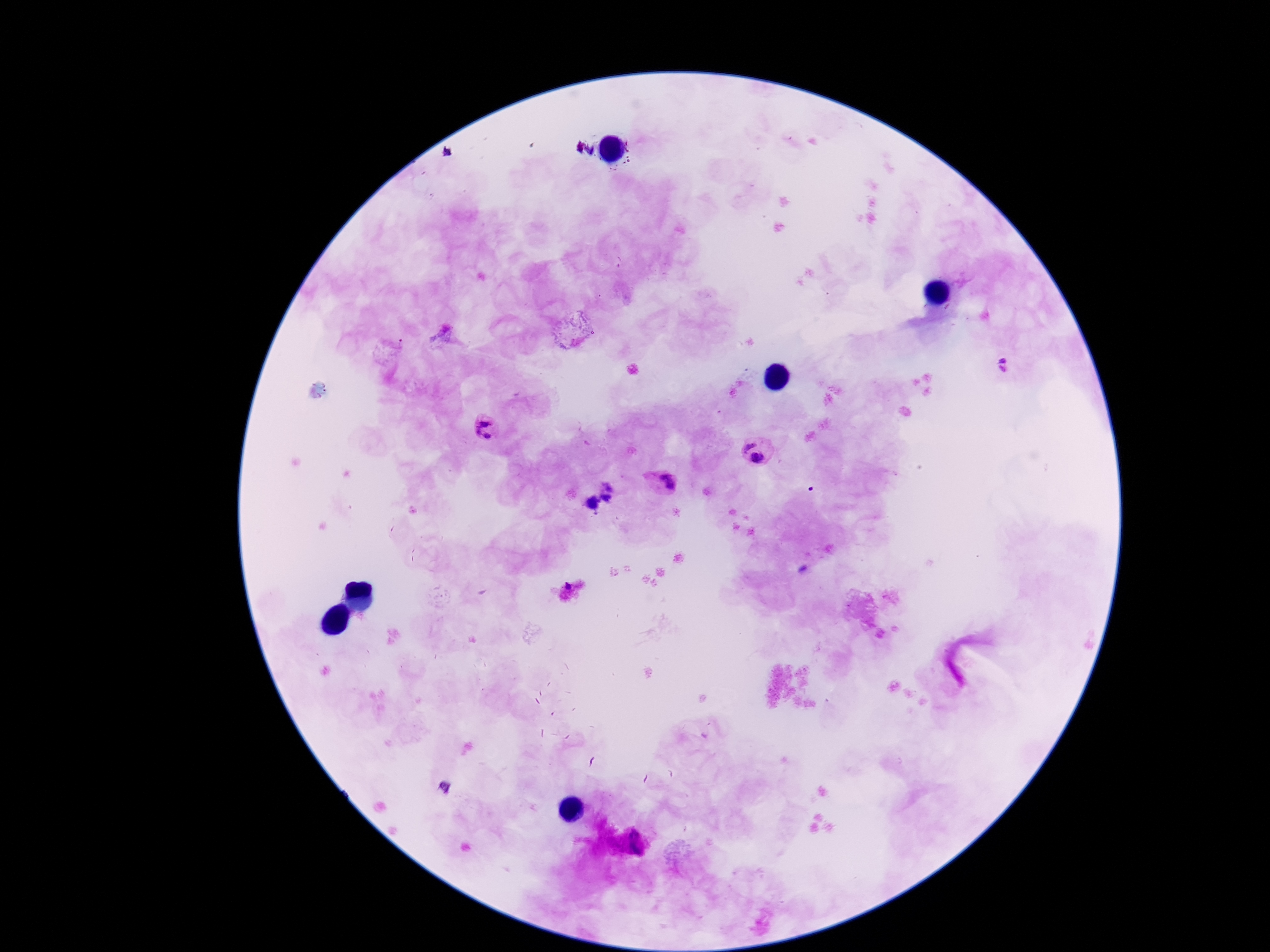

Approximate centers as [x, y] in pixels. Plasmodium parasite locations: [1006, 364], [489, 431], [747, 442], [760, 459], [665, 483], [639, 843]. 100x magnification. Photographed through the microscope eyepiece with a smartphone camera. Image is 1270×952 pixels. Giemsa stain. Patient malaria status: infected. Thick blood film. Single field of view.